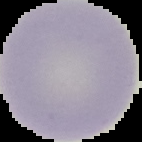

Summary:
  - Preparation: thin blood film
  - Malaria status: uninfected
  - Image type: cell region segmented out of the field of view; surrounding area masked to black
  - Image size: 142×142 pixels